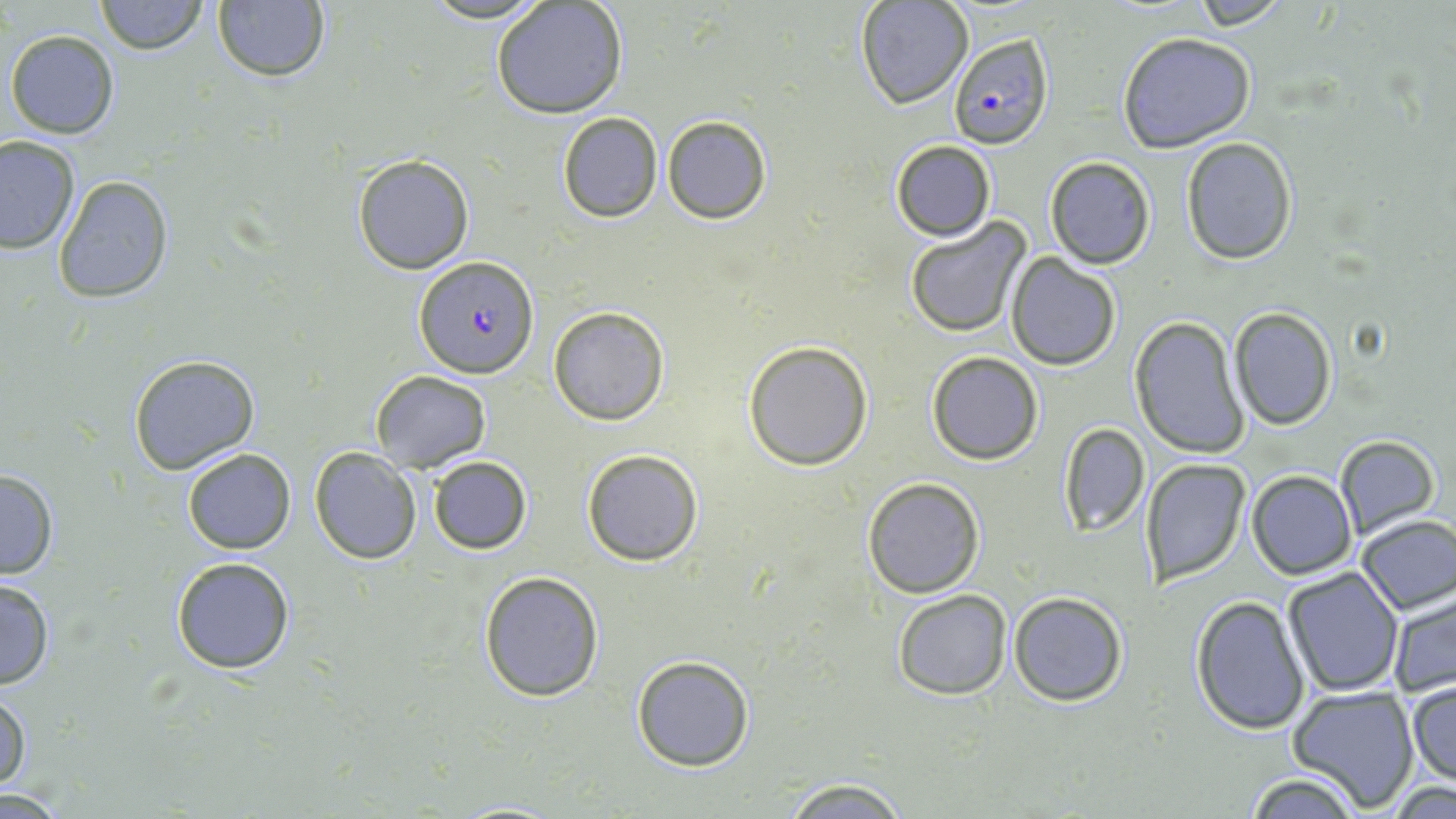
slide-level diagnosis = Plasmodium falciparum
image size = 1456×819 pixels
field of view = one of a larger specimen
uninfected red blood cell locations = approximate bounding boxes as named x1/y1/x2/y2 corners in pixels: (x1=95, y1=0, x2=207, y2=55), (x1=490, y1=0, x2=628, y2=119), (x1=1187, y1=0, x2=1299, y2=28), (x1=857, y1=1, x2=973, y2=109), (x1=210, y1=2, x2=333, y2=83), (x1=6, y1=29, x2=121, y2=140), (x1=1116, y1=32, x2=1258, y2=152), (x1=557, y1=112, x2=663, y2=222), (x1=661, y1=115, x2=772, y2=224), (x1=0, y1=136, x2=80, y2=255), (x1=1180, y1=136, x2=1297, y2=265), (x1=889, y1=138, x2=996, y2=240), (x1=351, y1=154, x2=475, y2=274), (x1=1044, y1=156, x2=1155, y2=269), (x1=53, y1=174, x2=174, y2=303), (x1=903, y1=217, x2=1031, y2=338), (x1=1005, y1=253, x2=1121, y2=370), (x1=548, y1=306, x2=669, y2=426), (x1=1229, y1=308, x2=1337, y2=429), (x1=1128, y1=315, x2=1250, y2=460), (x1=742, y1=340, x2=874, y2=470), (x1=925, y1=350, x2=1044, y2=465), (x1=129, y1=353, x2=260, y2=474), (x1=369, y1=369, x2=490, y2=472), (x1=1057, y1=422, x2=1150, y2=535), (x1=1333, y1=434, x2=1441, y2=538), (x1=311, y1=446, x2=422, y2=564), (x1=182, y1=447, x2=296, y2=554), (x1=581, y1=449, x2=704, y2=567), (x1=427, y1=455, x2=533, y2=555), (x1=1140, y1=459, x2=1251, y2=585), (x1=1246, y1=469, x2=1356, y2=580), (x1=0, y1=470, x2=60, y2=580), (x1=861, y1=476, x2=985, y2=598), (x1=1354, y1=515, x2=1456, y2=615), (x1=170, y1=556, x2=295, y2=674), (x1=1280, y1=568, x2=1404, y2=697), (x1=478, y1=570, x2=605, y2=703), (x1=0, y1=576, x2=56, y2=691), (x1=1386, y1=588, x2=1455, y2=701), (x1=892, y1=589, x2=1012, y2=699), (x1=1007, y1=591, x2=1129, y2=707), (x1=1189, y1=596, x2=1311, y2=734), (x1=630, y1=654, x2=756, y2=772), (x1=1406, y1=679, x2=1456, y2=789), (x1=1287, y1=685, x2=1419, y2=814), (x1=0, y1=687, x2=32, y2=794), (x1=1242, y1=770, x2=1363, y2=818), (x1=776, y1=777, x2=916, y2=819), (x1=1383, y1=779, x2=1456, y2=816), (x1=444, y1=800, x2=571, y2=817)
stain = May-Grünwald-Giemsa
preparation = thin blood film
modality = optical microscopy
Plasmodium falciparum-infected red blood cell locations = approximate bounding boxes as named x1/y1/x2/y2 corners in pixels: (x1=948, y1=31, x2=1056, y2=150), (x1=414, y1=254, x2=541, y2=378)
magnification = 1000x